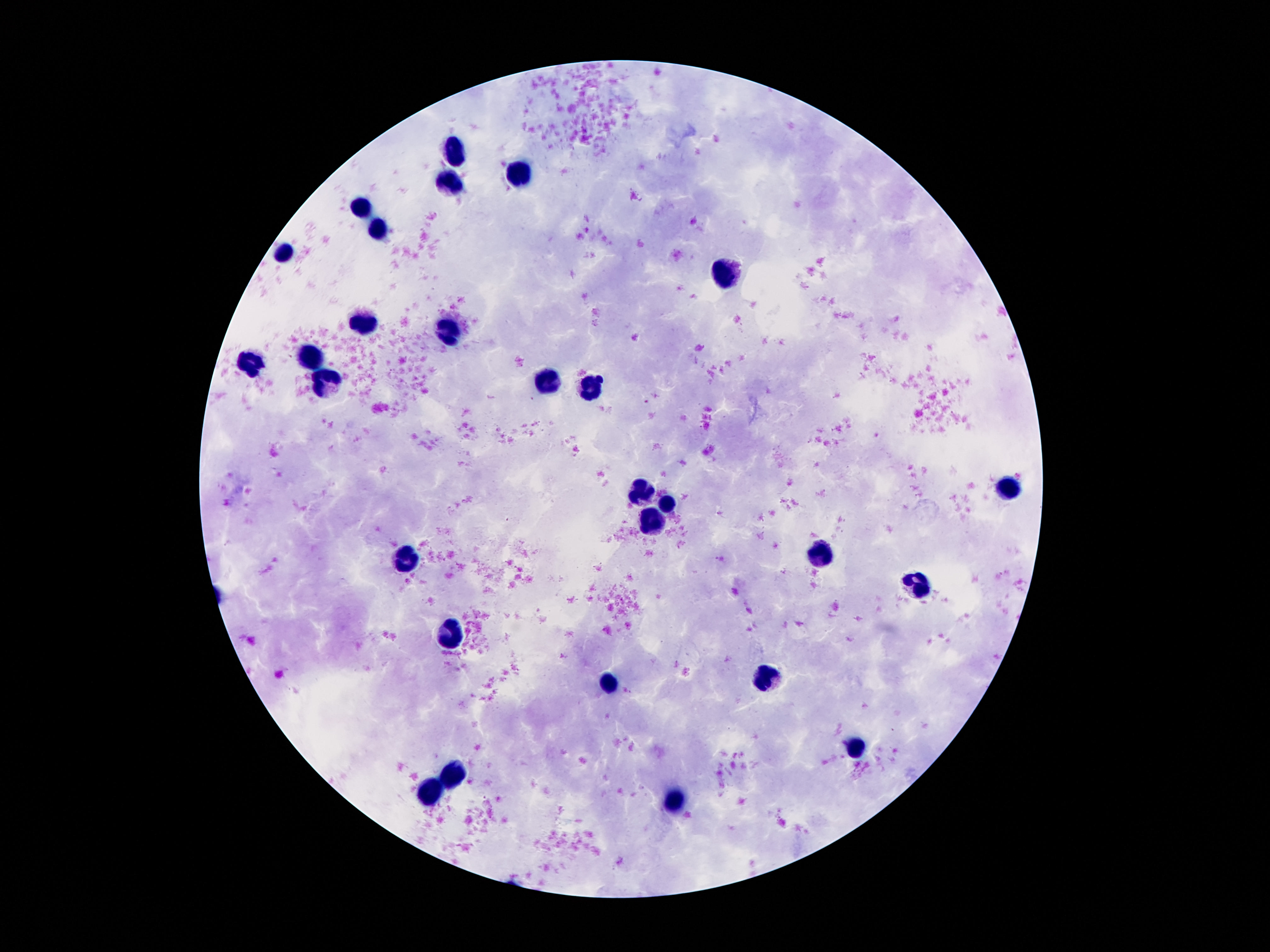

Approximate centers as (x, y) in pixels.
Summary:
  - Leukocyte locations: (456, 147), (515, 172), (449, 181), (362, 203), (381, 225), (281, 253), (723, 275), (362, 325), (449, 327), (312, 356), (250, 361), (328, 381), (549, 381), (593, 387), (1010, 486), (642, 496), (667, 499), (652, 524), (820, 555), (406, 561), (919, 583), (446, 632), (764, 673), (605, 682), (857, 750), (452, 770), (428, 797), (680, 801)
  - Field of view: one from this slide
  - Patient malaria status: uninfected
  - Magnification: 100x
  - Capture: smartphone camera through the microscope eyepiece
  - Preparation: thick peripheral-blood smear
  - Stain: Giemsa
  - Image size: 1270×952 pixels